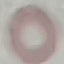
Summary:
  - Malaria status: uninfected
  - Capture: smartphone through the microscope eyepiece
  - Preparation: thin blood film
  - Stain: Giemsa
  - Image type: automatically extracted cell patch, resized to 64 × 64 pixels